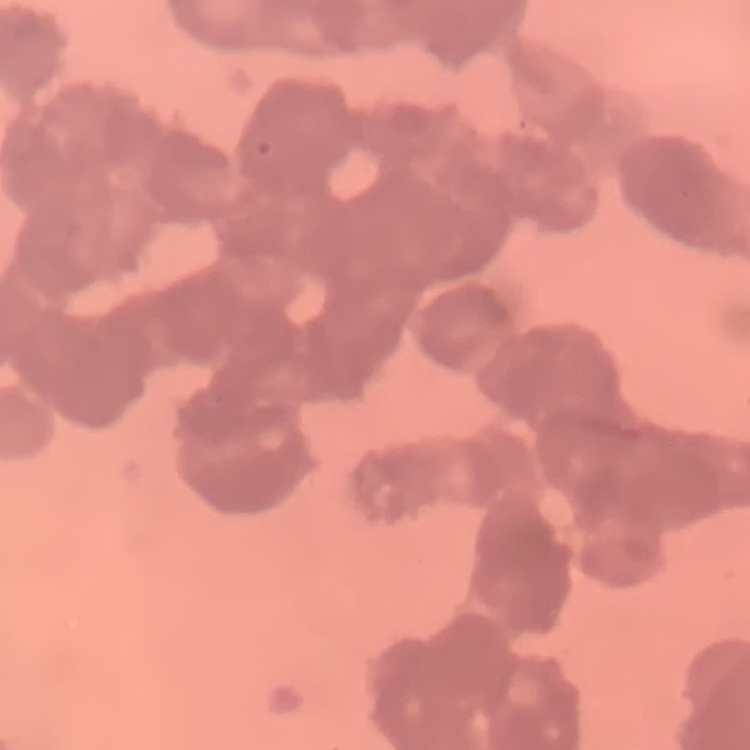
red blood cell morphology = rouleaux formation
stain = Field's or Giemsa
image type = one tile cut from a larger photomicrograph
preparation = thin blood film